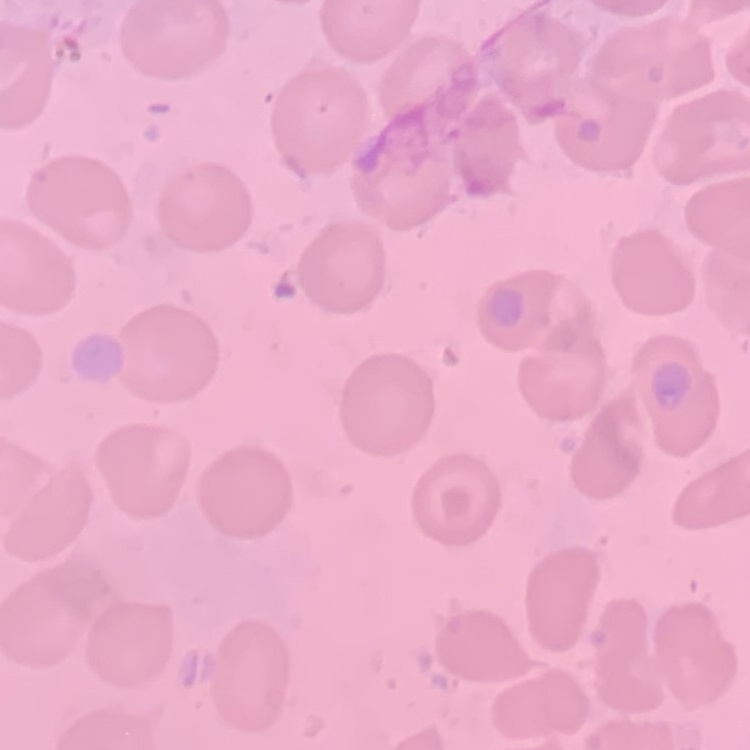
The red blood cells exhibit no rouleaux formation. Stained with either Field's or Giemsa. Thin blood smear. One tile cut from a larger photomicrograph.